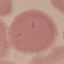 Result: no malaria parasites detected. Giemsa stain. Thin smear of blood. Photographed with a smartphone camera at the microscope eyepiece. Automatically extracted cell patch, resized to 64 × 64 pixels.